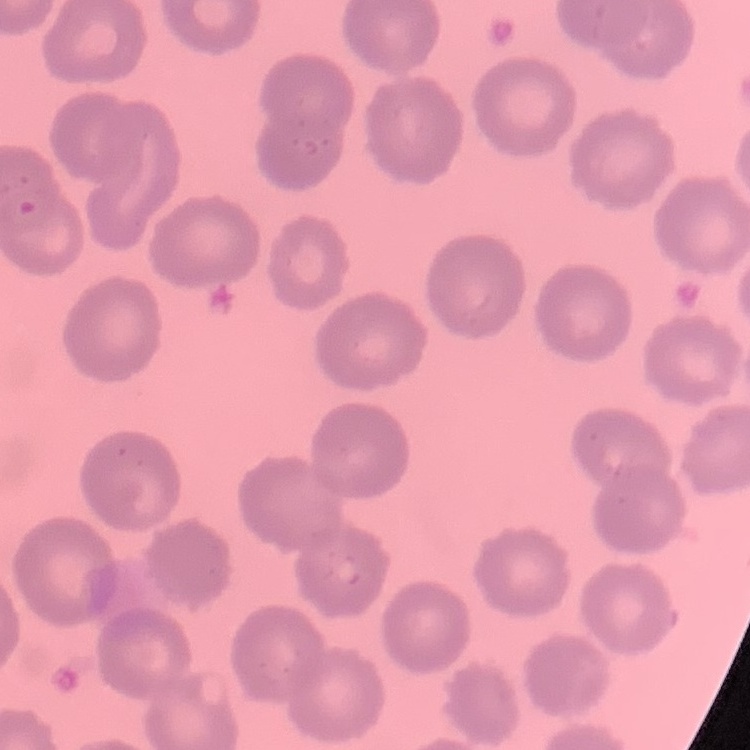
Summary:
  - Erythrocyte morphology: no rouleaux formation
  - Image type: square crop of a larger photomicrograph
  - Preparation: thin blood smear
  - Stain: Field's or Giemsa